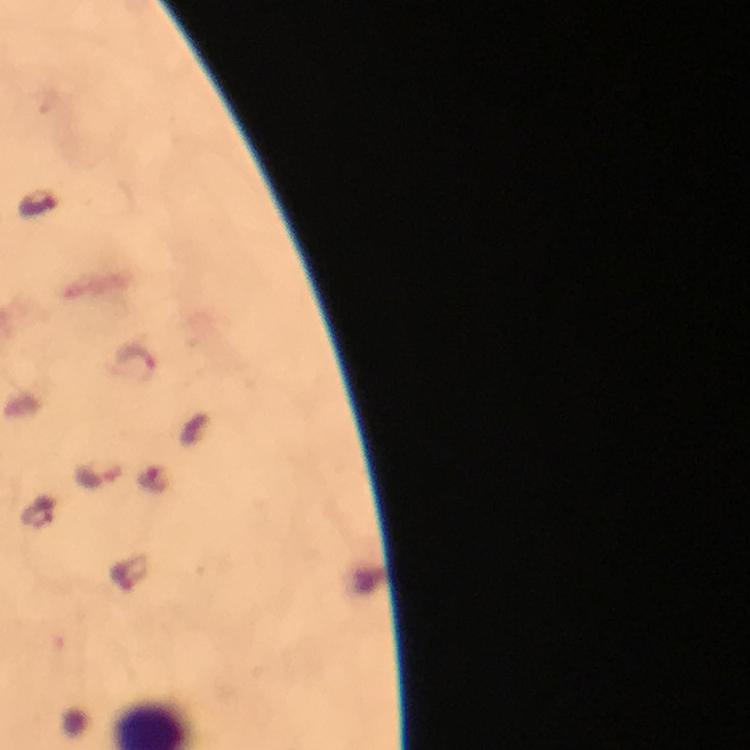
Approximate centers as {x, y} in pixels.
Summary:
  - Malaria parasite locations: {36, 203}, {136, 359}
  - Capture: smartphone camera through the microscope
  - Magnification: 100x
  - Cropped from: a single field of view
  - Stain: Giemsa
  - Image size: 750×750 pixels
  - Preparation: thick blood smear
  - Immersion oil: used
  - Context: from a diagnostic examination for malaria